Give a bounding box for every leukocyte visible.
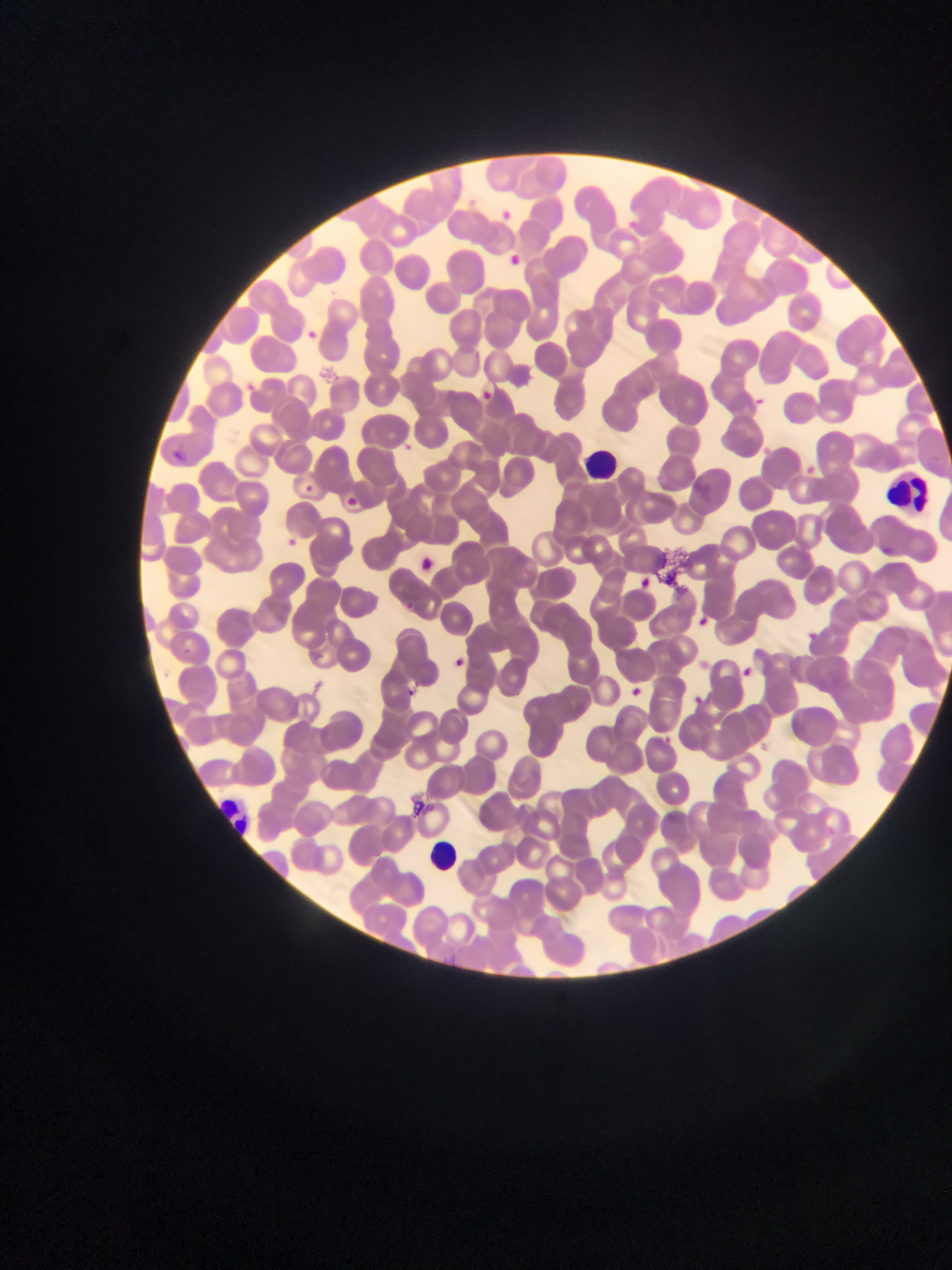
Approximate bounding boxes as {left, top, right, bottom} in pixels.
Leukocytes: {580, 444, 623, 487}, {883, 465, 942, 522}, {217, 791, 268, 840}, {414, 835, 472, 879}.

Plasmodium parasite locations: {493, 206, 517, 225}, {298, 325, 322, 347}, {472, 384, 499, 411}, {753, 394, 769, 408}, {765, 438, 781, 457}, {397, 440, 414, 456}, {170, 448, 193, 467}, {806, 460, 821, 483}, {299, 481, 318, 498}, {340, 493, 362, 511}, {283, 535, 307, 547}, {408, 552, 439, 578}, {633, 575, 656, 594}, {697, 613, 715, 630}, {805, 629, 819, 643}, {176, 646, 195, 662}, {453, 655, 475, 665}, {737, 663, 760, 675}, {623, 679, 657, 698}. Artifact (stain precipitate or debris) locations: {655, 545, 702, 589}, {399, 786, 432, 818}. Image is 952×1270 pixels. Thin blood film. Collected in Ghana. One field of view. Mobile-phone photograph taken through the microscope.